Give the extent of all Plasmodium malariae-infected red blood cells.
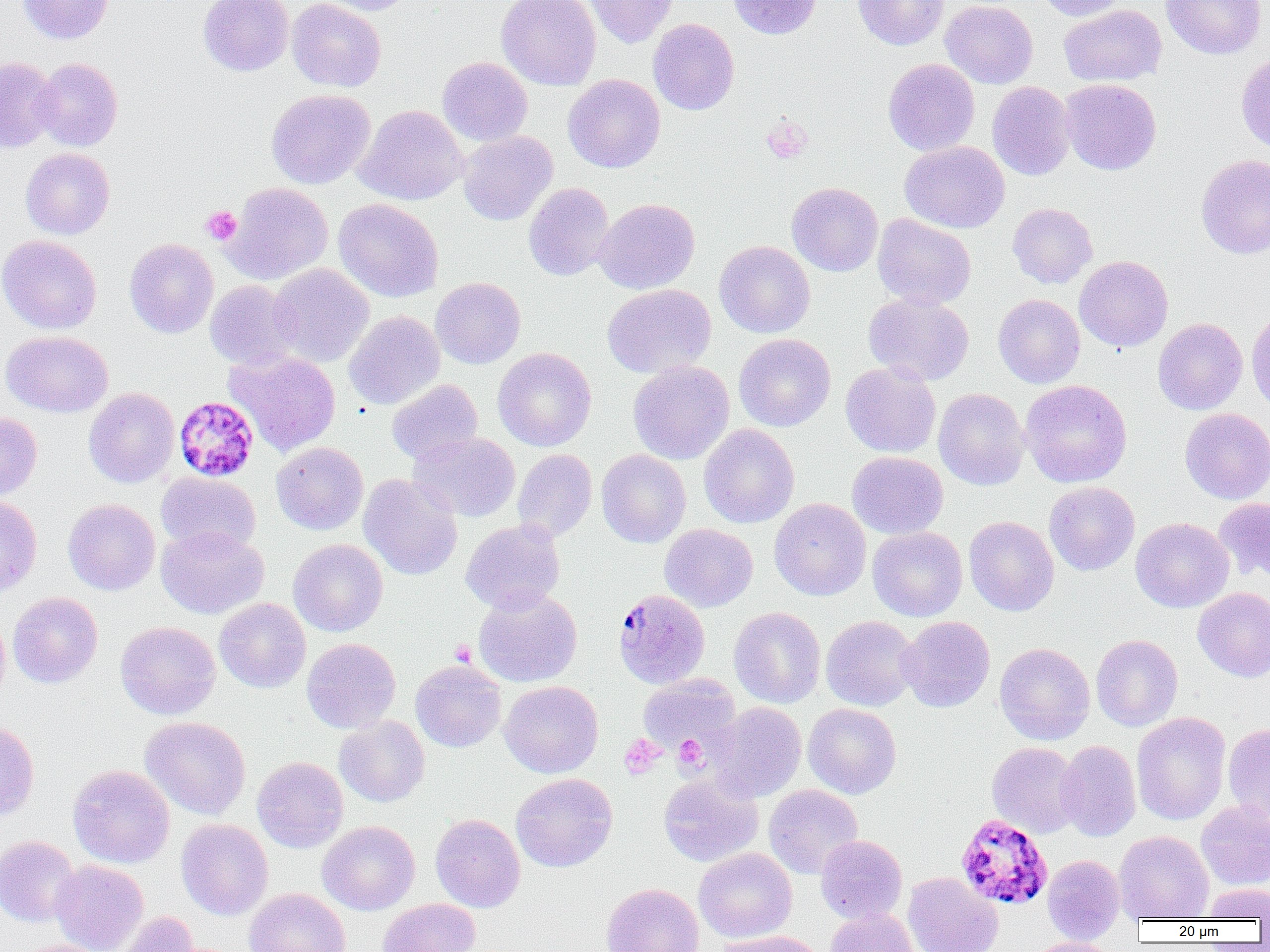
Approximate bounding boxes as [x1, y1, x2, y2] in pixels.
Plasmodium malariae-infected red blood cells: [173, 396, 259, 483], [612, 590, 710, 689], [956, 813, 1053, 911].

slide-level diagnosis = Plasmodium malariae
magnification = 1000x
platelet locations = approximate bounding boxes as [x1, y1, x2, y2] in pixels: [760, 115, 813, 164], [200, 206, 241, 245], [450, 640, 476, 666], [619, 735, 665, 779], [674, 735, 707, 770]
preparation = thin blood film
uninfected red blood cell locations = approximate bounding boxes as [x1, y1, x2, y2] in pixels: [18, 0, 114, 44], [198, 0, 294, 76], [287, 0, 386, 92], [309, 0, 416, 15], [497, 0, 601, 90], [583, 0, 679, 48], [727, 0, 823, 39], [853, 0, 949, 50], [940, 0, 1038, 88], [1037, 0, 1130, 20], [1161, 0, 1266, 60], [1059, 4, 1166, 87], [648, 18, 739, 115], [1236, 52, 1270, 155], [0, 56, 60, 153], [437, 57, 533, 147], [34, 58, 123, 151], [883, 58, 980, 156], [563, 74, 665, 173], [1060, 79, 1161, 175], [987, 81, 1076, 180], [265, 89, 375, 189], [355, 104, 468, 206], [458, 131, 558, 226], [900, 141, 1010, 233], [20, 148, 115, 239], [1195, 154, 1270, 259], [524, 182, 614, 281], [786, 182, 883, 276], [222, 183, 333, 285], [334, 198, 443, 302], [594, 198, 700, 294], [1007, 202, 1097, 289], [872, 214, 977, 309], [0, 234, 102, 334], [124, 238, 218, 338], [714, 240, 816, 338], [1074, 255, 1173, 352], [268, 263, 374, 368], [430, 277, 526, 368], [205, 280, 300, 370], [602, 284, 716, 378], [864, 292, 974, 385], [993, 294, 1085, 388], [1246, 306, 1270, 414], [343, 310, 445, 410], [1153, 318, 1248, 415], [1, 331, 113, 417], [734, 333, 836, 432], [493, 347, 596, 451], [225, 350, 342, 456], [628, 360, 734, 465], [840, 362, 941, 458], [387, 379, 483, 465], [1020, 380, 1132, 487], [83, 387, 180, 488], [933, 387, 1030, 490], [1180, 408, 1270, 504], [0, 412, 42, 501], [699, 424, 799, 528], [408, 432, 521, 522], [271, 441, 368, 535], [512, 449, 597, 542], [596, 449, 691, 548], [847, 451, 948, 539], [156, 472, 261, 556], [358, 474, 463, 580], [1044, 481, 1140, 575], [0, 494, 41, 599], [1214, 497, 1270, 584], [62, 498, 160, 595], [769, 498, 871, 600], [964, 516, 1059, 616], [1131, 517, 1234, 612], [460, 518, 566, 614], [660, 523, 758, 612], [156, 526, 269, 619], [867, 527, 967, 621], [288, 539, 387, 636], [1192, 587, 1270, 682], [472, 588, 582, 687], [7, 592, 103, 688], [214, 598, 311, 693], [729, 606, 826, 708], [0, 610, 10, 705], [820, 616, 919, 711], [898, 616, 995, 712], [115, 621, 221, 720], [1091, 634, 1183, 731], [301, 638, 401, 733], [995, 643, 1095, 745], [410, 660, 506, 752], [637, 674, 741, 753], [499, 680, 603, 778], [709, 702, 806, 802], [803, 703, 902, 799], [1132, 712, 1231, 825], [334, 715, 430, 807], [140, 716, 251, 819], [0, 720, 40, 821], [1223, 723, 1270, 826], [1056, 740, 1141, 841], [986, 742, 1082, 838], [252, 756, 348, 852], [68, 765, 175, 868], [511, 773, 617, 872], [659, 773, 763, 867], [763, 784, 863, 879], [1196, 800, 1270, 889], [430, 813, 525, 912], [176, 819, 273, 920], [317, 820, 420, 915], [1114, 830, 1214, 922], [815, 834, 907, 924], [0, 835, 81, 927], [693, 847, 797, 943], [1042, 854, 1124, 943], [50, 859, 148, 952], [903, 872, 1003, 952], [601, 883, 704, 952], [1202, 883, 1270, 921], [243, 888, 351, 952], [377, 898, 480, 952], [825, 907, 919, 952], [113, 911, 202, 952], [715, 930, 825, 952], [1024, 937, 1120, 952], [10, 939, 115, 952]
modality = optical microscopy
image size = 1270×952 pixels
field of view = single